Name the parasite shown.
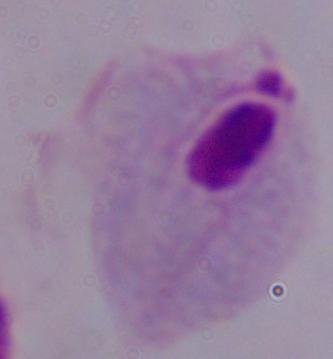
A trichomonad.

Summary:
  - Modality: micrograph
  - Magnification: 1000x